Report the malaria status of this cell.
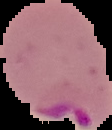
It is parasitized.

Image is 112×130 pixels. From a thin blood film. Segmented cell region on a black background.